Name the cell type shown.
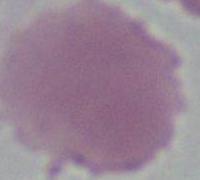

An erythrocyte.

modality = micrograph
magnification = 1000x